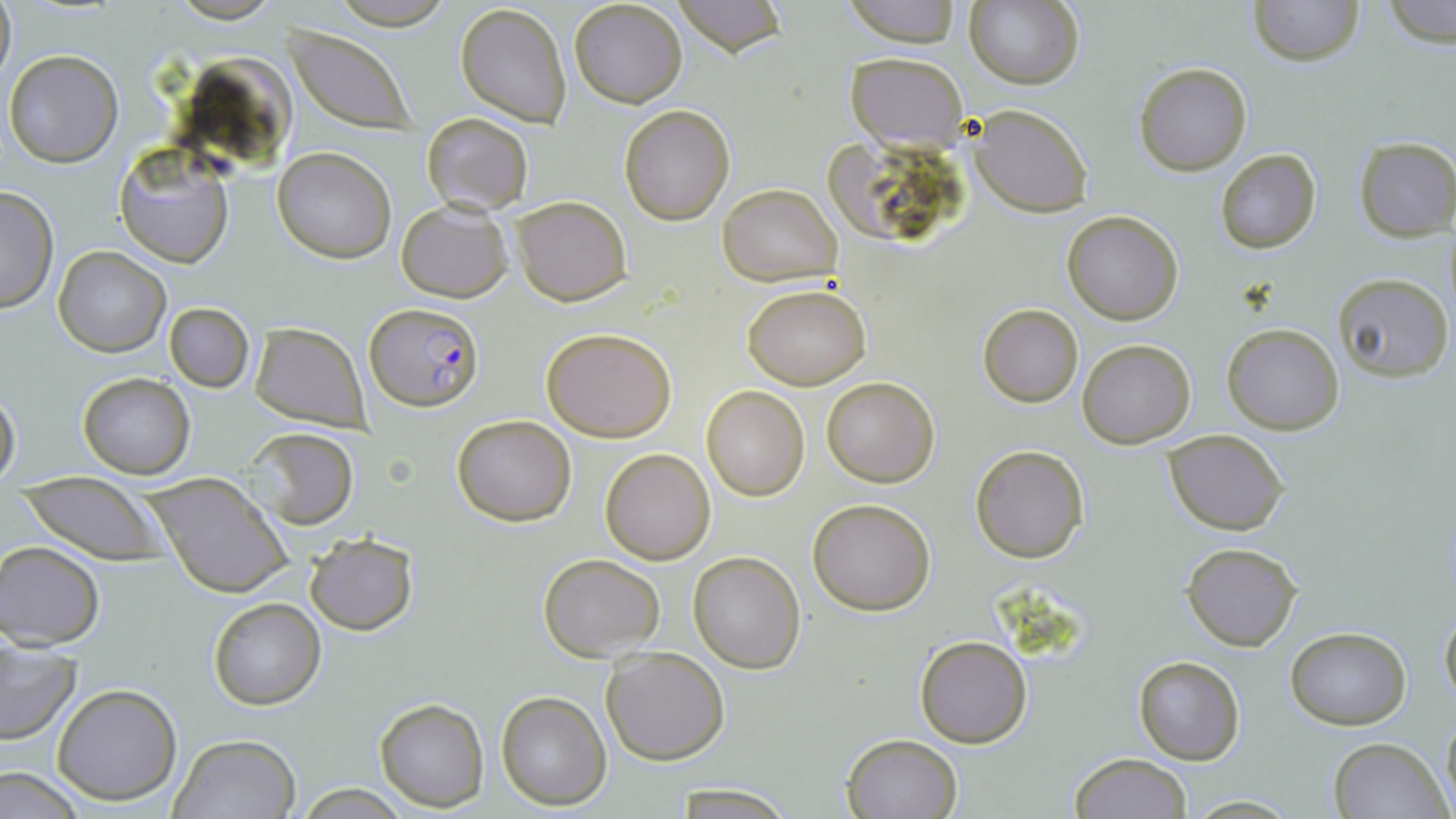

slide-level diagnosis = Plasmodium falciparum
stain = May-Grünwald-Giemsa
Plasmodium falciparum-infected red blood cell locations = approximate bounding boxes as named x1/y1/x2/y2 corners in pixels: (x1=365, y1=301, x2=483, y2=411)
magnification = 1000x
image size = 1456×819 pixels
field of view = single
uninfected red blood cell locations = approximate bounding boxes as named x1/y1/x2/y2 corners in pixels: (x1=1, y1=0, x2=16, y2=90), (x1=568, y1=0, x2=688, y2=108), (x1=673, y1=0, x2=786, y2=57), (x1=839, y1=0, x2=963, y2=46), (x1=967, y1=0, x2=1085, y2=91), (x1=1248, y1=0, x2=1364, y2=66), (x1=1383, y1=0, x2=1455, y2=50), (x1=455, y1=3, x2=572, y2=128), (x1=288, y1=28, x2=416, y2=133), (x1=4, y1=50, x2=122, y2=168), (x1=194, y1=50, x2=298, y2=160), (x1=846, y1=51, x2=968, y2=150), (x1=1134, y1=62, x2=1252, y2=175), (x1=968, y1=103, x2=1092, y2=217), (x1=618, y1=105, x2=737, y2=225), (x1=422, y1=111, x2=534, y2=216), (x1=1354, y1=138, x2=1456, y2=241), (x1=272, y1=147, x2=396, y2=262), (x1=1214, y1=147, x2=1322, y2=255), (x1=115, y1=148, x2=234, y2=269), (x1=718, y1=182, x2=841, y2=286), (x1=0, y1=186, x2=58, y2=315), (x1=512, y1=197, x2=630, y2=306), (x1=395, y1=198, x2=515, y2=302), (x1=1063, y1=210, x2=1183, y2=326), (x1=54, y1=246, x2=170, y2=357), (x1=1334, y1=274, x2=1452, y2=381), (x1=742, y1=283, x2=872, y2=389), (x1=164, y1=302, x2=255, y2=391), (x1=978, y1=303, x2=1083, y2=407), (x1=249, y1=322, x2=369, y2=428), (x1=1221, y1=322, x2=1346, y2=436), (x1=541, y1=327, x2=678, y2=442), (x1=1077, y1=339, x2=1196, y2=447), (x1=78, y1=372, x2=196, y2=478), (x1=822, y1=377, x2=939, y2=486), (x1=701, y1=385, x2=811, y2=501), (x1=0, y1=388, x2=20, y2=488), (x1=453, y1=415, x2=576, y2=527), (x1=247, y1=427, x2=358, y2=529), (x1=1163, y1=430, x2=1288, y2=534), (x1=969, y1=444, x2=1089, y2=564), (x1=601, y1=448, x2=715, y2=564), (x1=144, y1=473, x2=293, y2=599), (x1=22, y1=477, x2=164, y2=564), (x1=807, y1=498, x2=937, y2=615), (x1=304, y1=533, x2=417, y2=636), (x1=1181, y1=541, x2=1303, y2=651), (x1=0, y1=542, x2=104, y2=649), (x1=688, y1=551, x2=806, y2=674), (x1=538, y1=553, x2=665, y2=661), (x1=207, y1=598, x2=324, y2=710), (x1=1439, y1=602, x2=1456, y2=706), (x1=1284, y1=627, x2=1412, y2=729), (x1=0, y1=632, x2=81, y2=747), (x1=914, y1=635, x2=1033, y2=749), (x1=601, y1=646, x2=729, y2=765), (x1=1132, y1=655, x2=1245, y2=765), (x1=51, y1=683, x2=183, y2=805), (x1=495, y1=689, x2=611, y2=810), (x1=374, y1=696, x2=489, y2=810), (x1=1441, y1=705, x2=1456, y2=813), (x1=840, y1=732, x2=963, y2=819), (x1=170, y1=733, x2=300, y2=817), (x1=1327, y1=737, x2=1451, y2=819), (x1=1069, y1=752, x2=1193, y2=818), (x1=0, y1=764, x2=89, y2=818), (x1=294, y1=784, x2=414, y2=817), (x1=664, y1=785, x2=800, y2=818), (x1=1184, y1=794, x2=1299, y2=817)
modality = optical microscopy
preparation = thin blood film